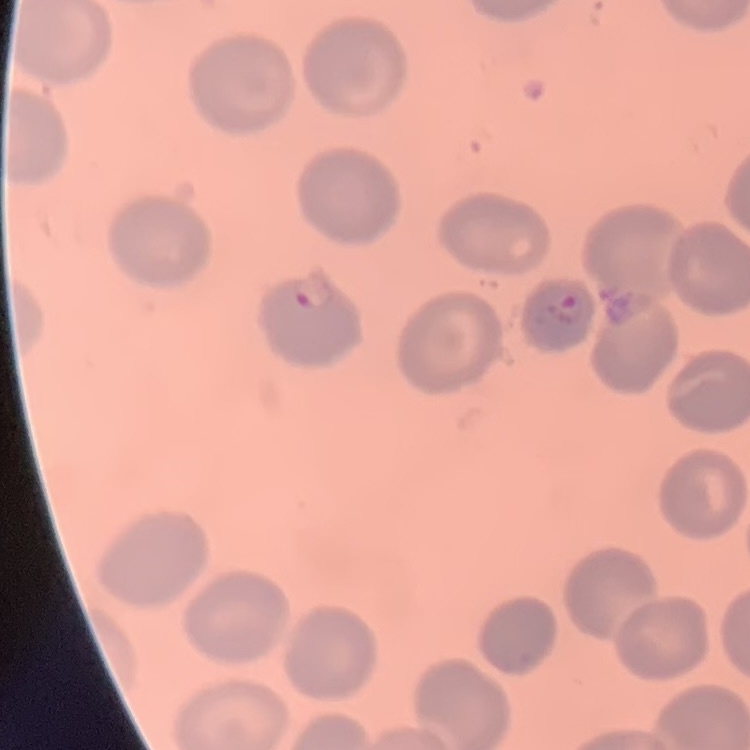
The red blood cells show no rouleaux formation. Stained with either Field's or Giemsa. Thin peripheral smear. One tile cut from a larger photomicrograph.